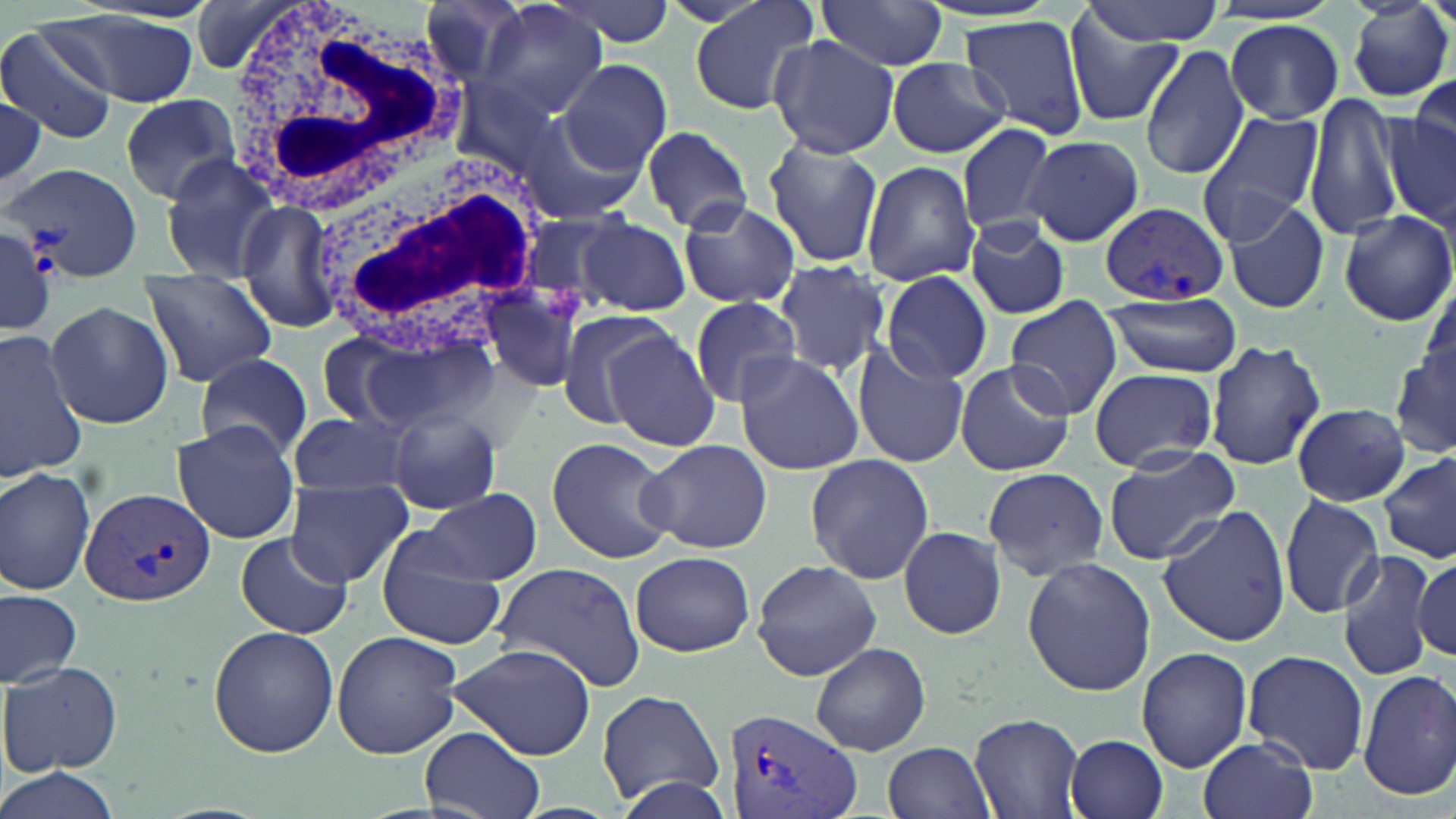

slide-level diagnosis = Plasmodium vivax
image size = 1456×819 pixels
Plasmodium vivax-infected red blood cell locations = approximate bounding boxes as [x1, y1, x2, y2] in pixels: [3, 160, 144, 280], [1100, 202, 1229, 308], [79, 486, 217, 608], [723, 707, 861, 819]
white blood cell locations = approximate bounding boxes as [x1, y1, x2, y2] in pixels: [229, 5, 468, 218], [307, 151, 548, 361]
uninfected red blood cell locations = approximate bounding boxes as [x1, y1, x2, y2] in pixels: [418, 0, 536, 88], [476, 0, 611, 121], [687, 0, 825, 116], [1078, 0, 1228, 45], [551, 1, 674, 48], [814, 1, 949, 75], [1349, 1, 1452, 103], [47, 13, 200, 108], [960, 15, 1092, 141], [1066, 16, 1182, 125], [1224, 19, 1344, 124], [2, 24, 120, 145], [769, 34, 900, 158], [1137, 43, 1248, 180], [887, 56, 1011, 159], [557, 60, 673, 175], [1408, 78, 1456, 166], [1305, 91, 1407, 241], [0, 93, 48, 198], [118, 93, 240, 203], [1382, 106, 1456, 233], [515, 109, 644, 223], [1195, 110, 1324, 243], [953, 121, 1059, 239], [639, 124, 753, 235], [1023, 135, 1143, 246], [764, 136, 884, 269], [158, 151, 289, 283], [860, 162, 979, 286], [236, 198, 342, 333], [675, 198, 800, 309], [1224, 199, 1331, 315], [1338, 209, 1456, 327], [517, 213, 629, 318], [964, 217, 1069, 319], [575, 218, 692, 315], [0, 223, 56, 339], [772, 259, 889, 376], [881, 269, 991, 384], [140, 273, 278, 387], [479, 283, 586, 394], [1101, 290, 1245, 376], [1005, 296, 1125, 421], [689, 297, 804, 408], [44, 299, 173, 429], [552, 308, 675, 429], [344, 324, 497, 432], [311, 329, 424, 430], [1, 330, 88, 480], [602, 330, 721, 452], [1204, 340, 1325, 470], [1393, 343, 1455, 461], [851, 344, 970, 469], [732, 350, 864, 475], [196, 353, 314, 459], [955, 359, 1075, 476], [1089, 367, 1218, 471], [1292, 404, 1411, 505], [385, 406, 503, 516], [287, 411, 414, 501], [172, 422, 299, 543], [547, 436, 673, 564], [638, 438, 773, 554], [1103, 447, 1241, 566], [1379, 452, 1456, 564], [804, 456, 934, 584], [0, 465, 97, 596], [983, 467, 1108, 579], [286, 479, 412, 586], [423, 488, 542, 585], [1280, 494, 1386, 618], [1157, 504, 1290, 648], [898, 525, 1006, 640], [373, 529, 506, 649], [234, 532, 355, 640], [1337, 548, 1437, 684], [630, 550, 755, 657], [1413, 555, 1455, 662], [1021, 557, 1156, 694], [752, 559, 883, 681], [491, 565, 646, 689], [0, 589, 81, 688], [208, 626, 338, 759], [331, 629, 462, 759], [808, 641, 931, 755], [447, 643, 596, 758], [1135, 647, 1251, 772], [1243, 648, 1370, 775], [2, 660, 123, 775], [1357, 668, 1456, 799], [595, 689, 728, 807], [968, 712, 1086, 819], [418, 726, 547, 819], [1065, 733, 1169, 819], [1197, 736, 1317, 819], [884, 741, 996, 819], [0, 765, 119, 819], [609, 774, 734, 819]
modality = light microscopy
stain = May-Grünwald-Giemsa
field of view = one of a larger specimen
preparation = thin blood smear
magnification = 1000x